Comment on the morphology of the red blood cells.
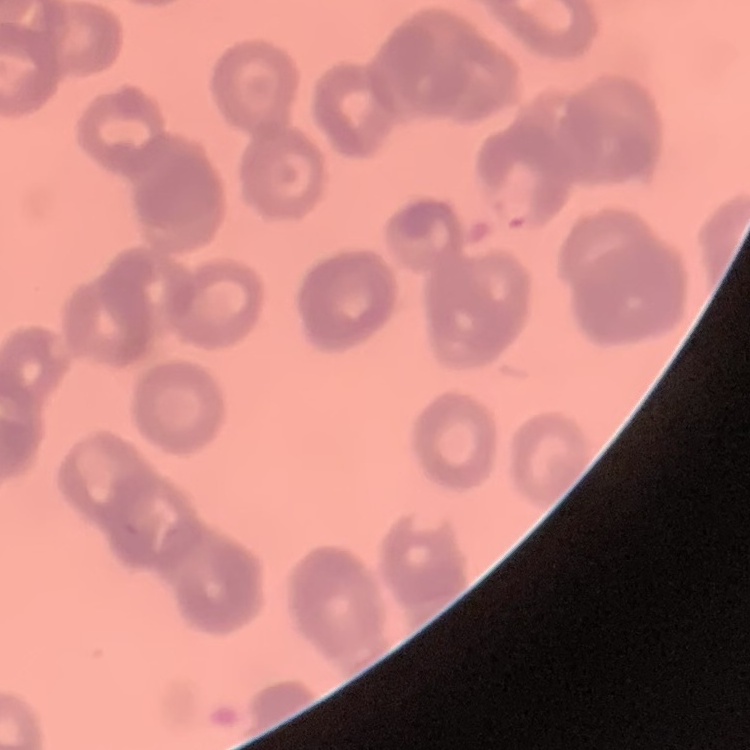
They show rouleaux formation.

image type = square crop of a larger photomicrograph
stain = Field's or Giemsa
preparation = thin blood smear